Assess for malaria.
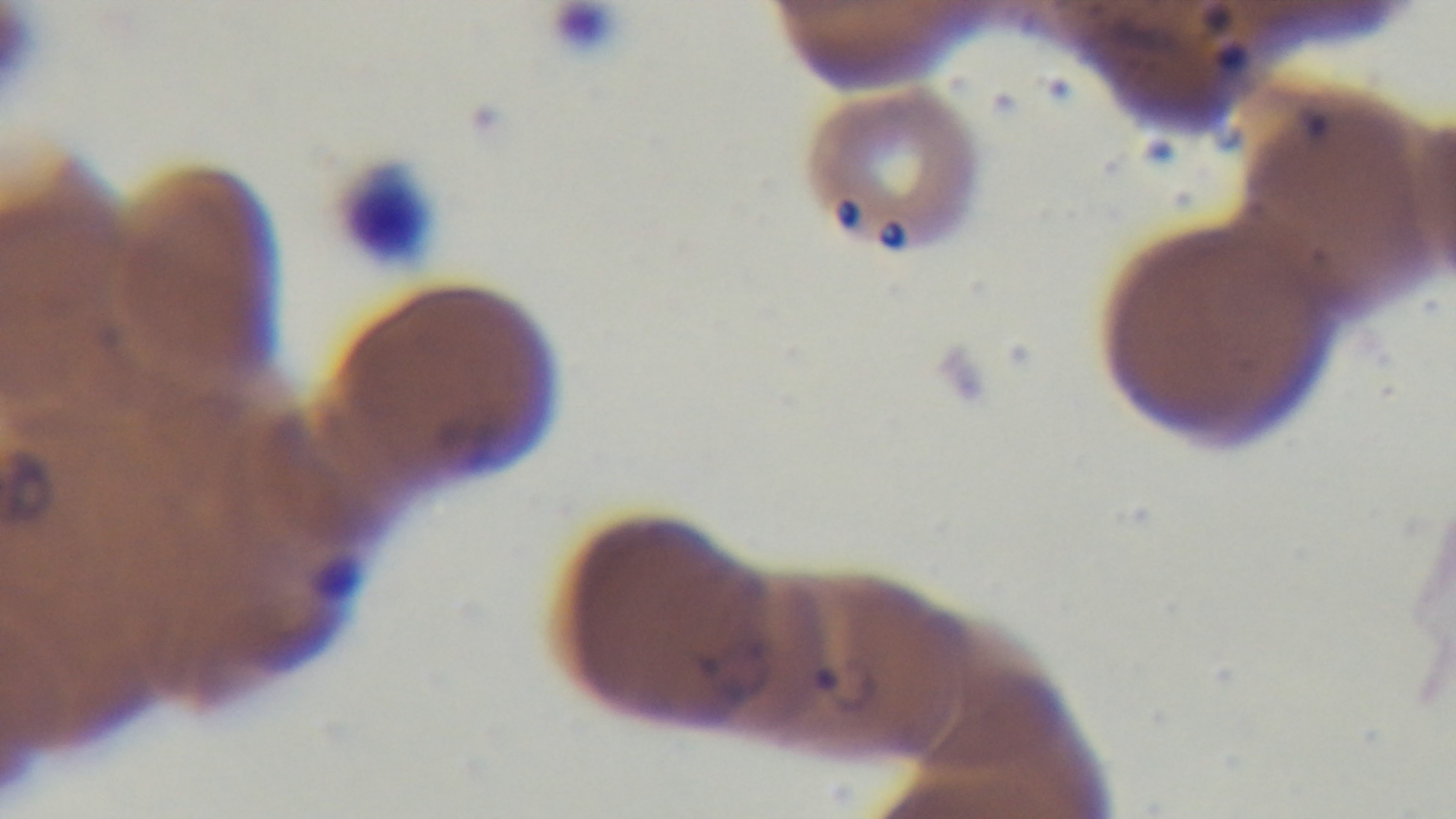
Positive.

Summary:
  - Objective: 100x oil immersion
  - Preparation: thin
  - Modality: light microscopy
  - Field of view: one from the slide
  - Stain: Giemsa
  - Capture: mounted 4K digital camera